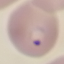
Result: malaria parasites identified. Acquired by smartphone through the microscope eyepiece. Thin smear of blood. Cell patch, automatically extracted from a larger field of view and resized to 64 × 64 pixels. Giemsa-stained preparation.